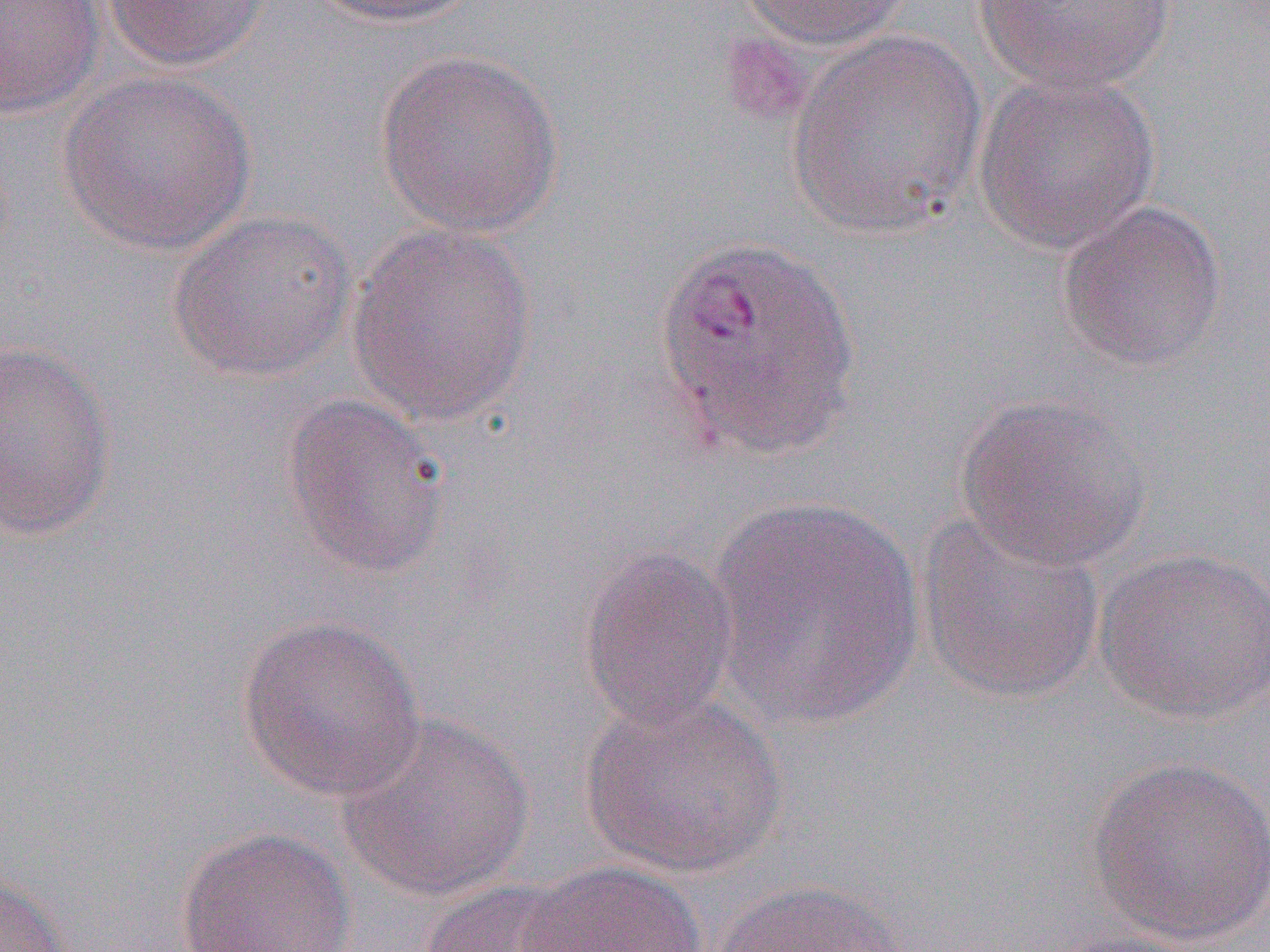
Approximate bounding boxes as (x1, y1, x2, y2) in pixels. Platelet locations: (718, 31, 814, 128). Uninfected red blood cell locations: (0, 0, 107, 119), (101, 0, 275, 70), (305, 0, 486, 28), (734, 0, 915, 51), (968, 0, 1179, 96), (784, 29, 989, 239), (373, 47, 565, 237), (970, 67, 1162, 255), (57, 70, 258, 256), (1055, 200, 1229, 371), (167, 208, 358, 382), (345, 221, 540, 428), (0, 338, 119, 542), (952, 391, 1154, 572), (280, 393, 452, 580), (707, 497, 927, 732), (914, 509, 1107, 707), (577, 543, 742, 734), (1094, 546, 1270, 724), (235, 613, 428, 802), (576, 690, 790, 880), (335, 712, 537, 901), (1085, 755, 1270, 947), (173, 826, 357, 952), (512, 861, 708, 951), (0, 870, 74, 951), (711, 879, 912, 952), (419, 880, 589, 952), (1041, 928, 1209, 952). Slide-level diagnosis: Plasmodium vivax. Captured at 1000x magnification. Image is 1270×952 pixels. Thin blood smear. One field of a larger specimen. Optical microscopy.